Identify the blood parasite species.
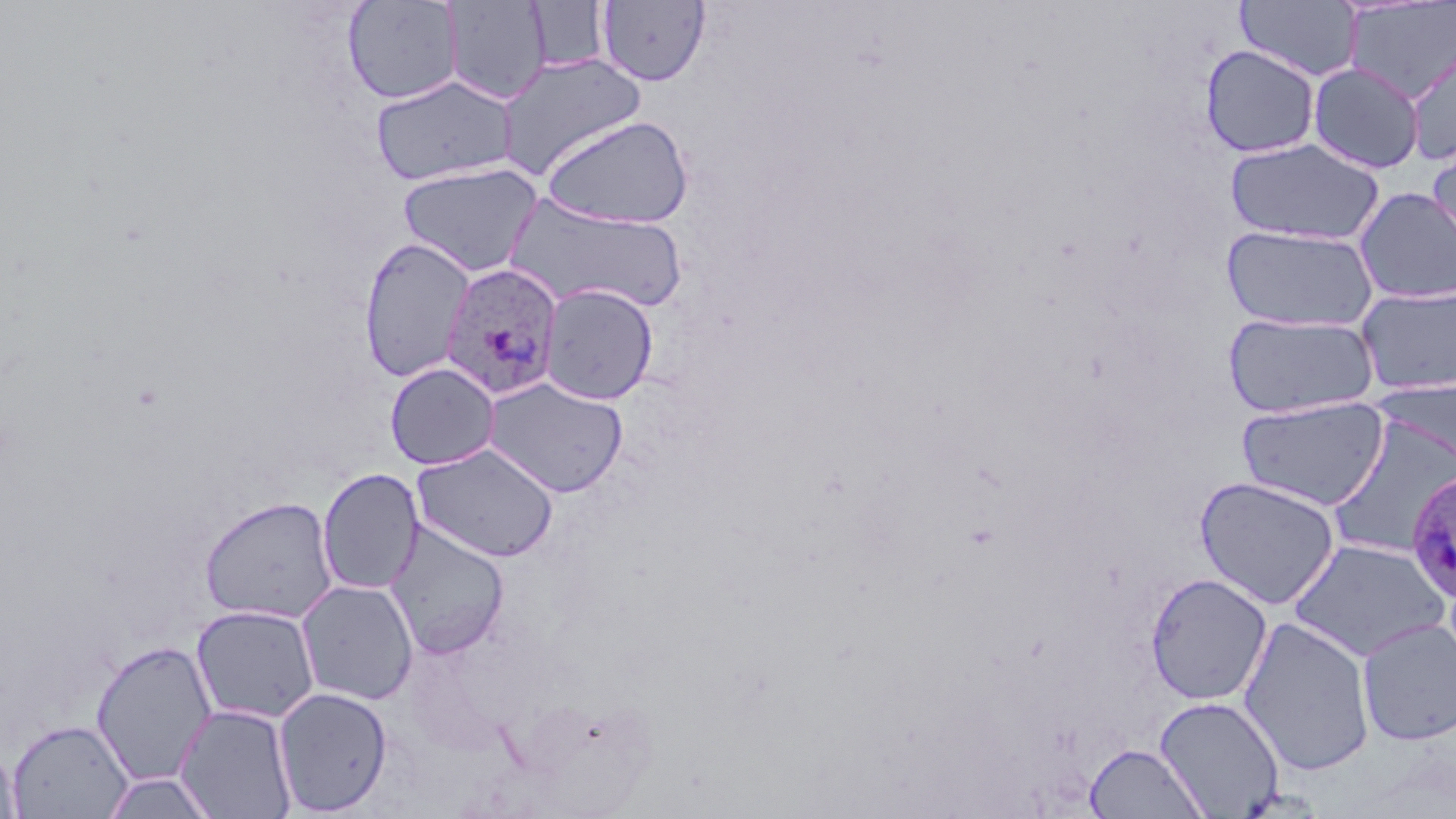
Plasmodium ovale.

Approximate bounding boxes as (x1,y1)-(x2,y2) corner pairs in pixels. Plasmodium ovale-infected red blood cell locations: (440,263)-(564,400), (1404,469)-(1456,606). Uninfected red blood cell locations: (342,0)-(462,105), (597,0)-(710,86), (442,1)-(551,106), (527,1)-(610,73), (1235,1)-(1364,83), (1343,1)-(1456,103), (1405,39)-(1456,163), (1200,44)-(1320,159), (495,53)-(648,180), (1308,62)-(1425,174), (370,75)-(519,187), (539,115)-(694,229), (1225,137)-(1385,246), (1427,139)-(1456,260), (397,162)-(545,277), (1354,186)-(1456,305), (503,192)-(688,315), (1222,224)-(1378,333), (359,236)-(474,382), (538,283)-(659,405), (1356,285)-(1456,396), (1222,312)-(1381,419), (385,362)-(500,470), (397,366)-(524,558), (1375,374)-(1456,477), (482,376)-(629,498), (1237,396)-(1390,511), (1326,416)-(1456,562), (411,442)-(560,563), (317,468)-(424,596), (1194,475)-(1341,610), (198,495)-(338,625), (384,519)-(511,659), (1287,538)-(1450,662), (1145,572)-(1273,705), (296,579)-(419,706), (191,605)-(321,725), (1239,615)-(1376,776), (1357,618)-(1456,746), (90,640)-(217,786), (273,686)-(393,815), (1155,695)-(1285,818), (175,703)-(298,819), (7,719)-(134,819), (0,739)-(21,819), (1085,742)-(1208,818), (100,771)-(219,818). May-Grünwald-Giemsa stain. Thin blood film. 1000x magnification. Light microscopy. Single field of view. Image is 1456×819 pixels.